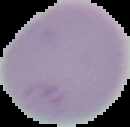
result: negative for malaria parasites
image_size: 130×127 pixels
preparation: thin blood smear
image_type: cell region segmented out of the field of view; surrounding area masked to black